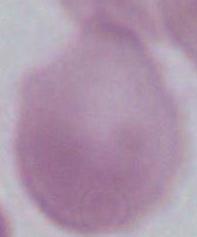
magnification = 1000x
modality = micrograph
identification = red blood cell